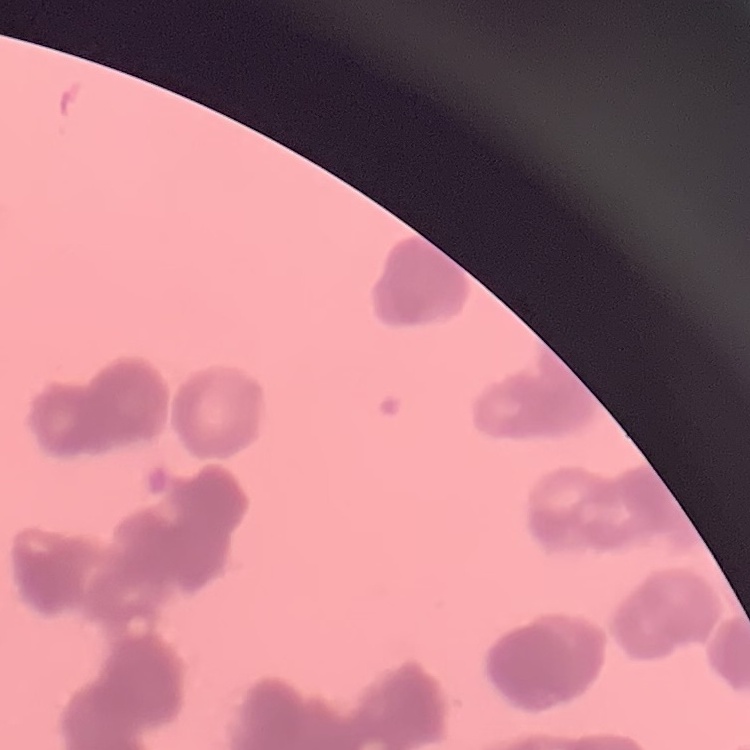

red blood cell morphology = rouleaux formation
stain = Field's or Giemsa
preparation = thin peripheral smear
image type = one tile cut from a larger photomicrograph